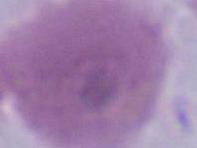
modality = photomicrograph
magnification = 1000x
identification = erythrocyte